Locate every Plasmodium vivax-infected red blood cell.
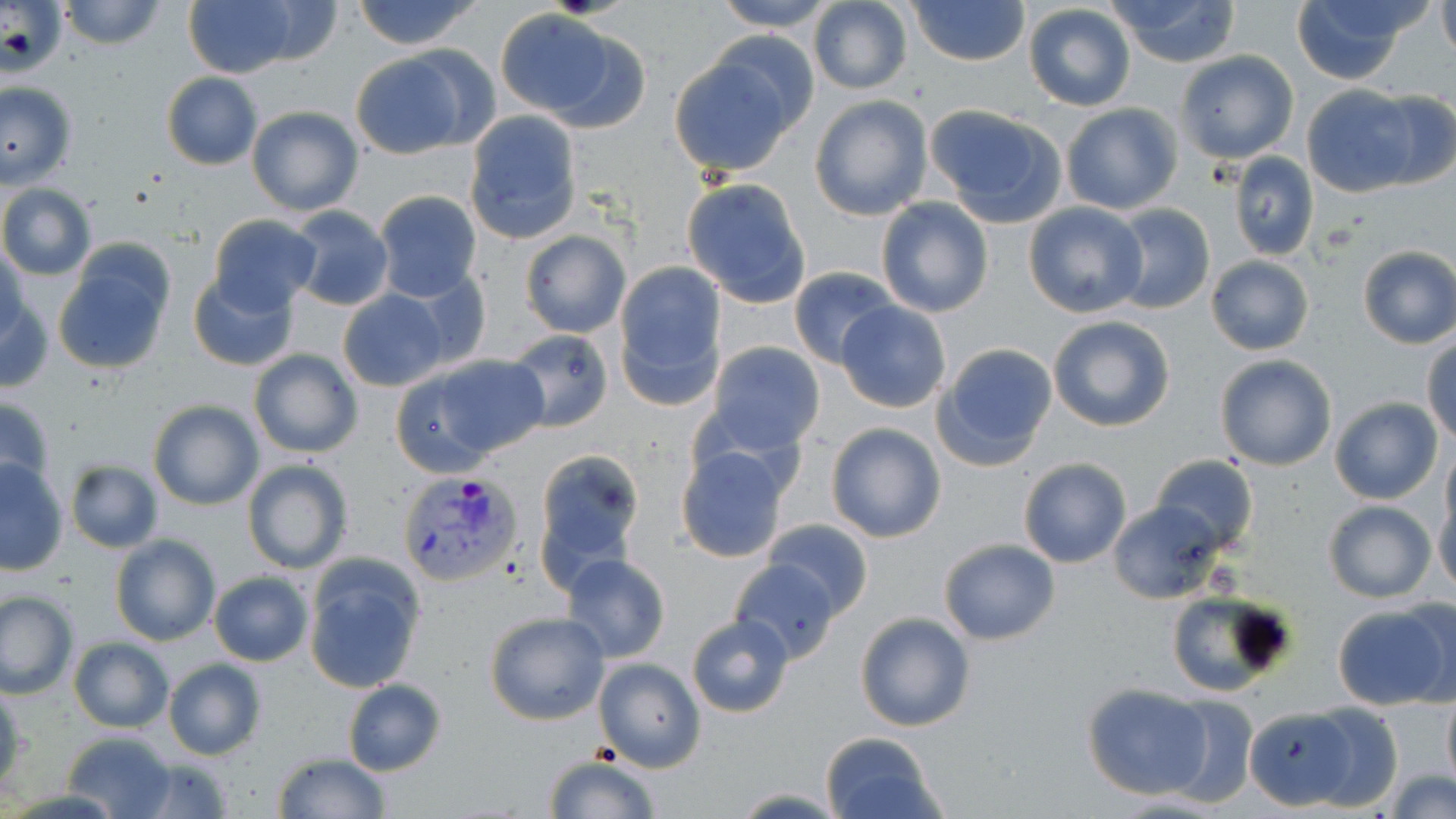
Approximate bounding boxes as named x1/y1/x2/y2 corners in pixels.
Plasmodium vivax-infected red blood cells: (x1=398, y1=471, x2=525, y2=588).

slide_level_diagnosis: Plasmodium vivax
field_of_view: single
uninfected_red_blood_cell_locations: 'approximate bounding boxes as named x1/y1/x2/y2 corners in pixels: (x1=58, y1=0, x2=166, y2=49), (x1=351, y1=0, x2=484, y2=51), (x1=710, y1=0, x2=840, y2=32), (x1=909, y1=0, x2=1029, y2=67), (x1=1108, y1=0, x2=1242, y2=68), (x1=1290, y1=0, x2=1420, y2=85), (x1=806, y1=1, x2=913, y2=93), (x1=1436, y1=1, x2=1456, y2=62), (x1=184, y1=2, x2=298, y2=78), (x1=1023, y1=4, x2=1137, y2=112), (x1=494, y1=13, x2=646, y2=131), (x1=668, y1=49, x2=800, y2=177), (x1=349, y1=50, x2=478, y2=159), (x1=1173, y1=51, x2=1299, y2=165), (x1=161, y1=73, x2=264, y2=170), (x1=0, y1=82, x2=77, y2=188), (x1=1300, y1=85, x2=1424, y2=197), (x1=1361, y1=89, x2=1456, y2=192), (x1=808, y1=95, x2=933, y2=220), (x1=1060, y1=103, x2=1183, y2=215), (x1=925, y1=105, x2=1067, y2=227), (x1=246, y1=106, x2=363, y2=216), (x1=464, y1=111, x2=582, y2=242), (x1=1229, y1=153, x2=1319, y2=261), (x1=682, y1=177, x2=812, y2=308), (x1=1, y1=183, x2=97, y2=280), (x1=373, y1=191, x2=482, y2=301), (x1=875, y1=197, x2=994, y2=317), (x1=1022, y1=201, x2=1149, y2=319), (x1=1106, y1=204, x2=1215, y2=314), (x1=286, y1=206, x2=395, y2=311), (x1=208, y1=215, x2=323, y2=315), (x1=518, y1=231, x2=630, y2=339), (x1=1, y1=246, x2=31, y2=339), (x1=1356, y1=246, x2=1456, y2=349), (x1=52, y1=250, x2=174, y2=374), (x1=1205, y1=255, x2=1314, y2=355), (x1=613, y1=262, x2=726, y2=409), (x1=789, y1=267, x2=902, y2=370), (x1=188, y1=270, x2=299, y2=371), (x1=392, y1=271, x2=492, y2=373), (x1=337, y1=288, x2=450, y2=392), (x1=1, y1=289, x2=52, y2=393), (x1=836, y1=301, x2=951, y2=413), (x1=1047, y1=315, x2=1177, y2=432), (x1=503, y1=328, x2=614, y2=432), (x1=1423, y1=334, x2=1456, y2=445), (x1=708, y1=342, x2=826, y2=454), (x1=932, y1=343, x2=1058, y2=469), (x1=248, y1=349, x2=362, y2=459), (x1=429, y1=354, x2=551, y2=460), (x1=1214, y1=355, x2=1338, y2=471), (x1=388, y1=365, x2=505, y2=478), (x1=0, y1=396, x2=56, y2=498), (x1=1330, y1=398, x2=1443, y2=505), (x1=147, y1=399, x2=263, y2=511), (x1=825, y1=422, x2=946, y2=543), (x1=1442, y1=444, x2=1456, y2=539), (x1=675, y1=446, x2=791, y2=563), (x1=533, y1=450, x2=646, y2=580), (x1=1151, y1=454, x2=1258, y2=554), (x1=1017, y1=458, x2=1132, y2=568), (x1=0, y1=460, x2=69, y2=573), (x1=242, y1=460, x2=354, y2=575), (x1=65, y1=461, x2=163, y2=552), (x1=1433, y1=493, x2=1456, y2=600), (x1=1106, y1=499, x2=1225, y2=605), (x1=1322, y1=499, x2=1437, y2=603), (x1=764, y1=518, x2=873, y2=617), (x1=109, y1=534, x2=220, y2=646), (x1=939, y1=537, x2=1060, y2=645), (x1=300, y1=554, x2=429, y2=693), (x1=561, y1=554, x2=671, y2=663), (x1=730, y1=558, x2=839, y2=663), (x1=208, y1=572, x2=314, y2=667), (x1=1165, y1=589, x2=1293, y2=695), (x1=1, y1=591, x2=78, y2=698), (x1=1395, y1=596, x2=1456, y2=705), (x1=1332, y1=604, x2=1453, y2=711), (x1=484, y1=610, x2=610, y2=725), (x1=855, y1=612, x2=976, y2=732), (x1=686, y1=613, x2=795, y2=717), (x1=69, y1=638, x2=174, y2=731), (x1=592, y1=657, x2=705, y2=772), (x1=162, y1=660, x2=267, y2=761), (x1=343, y1=679, x2=446, y2=776), (x1=1082, y1=682, x2=1215, y2=799), (x1=0, y1=688, x2=27, y2=799), (x1=1441, y1=689, x2=1456, y2=792), (x1=1157, y1=693, x2=1259, y2=808), (x1=1301, y1=705, x2=1405, y2=811), (x1=1245, y1=707, x2=1359, y2=810), (x1=60, y1=732, x2=179, y2=819), (x1=820, y1=732, x2=945, y2=819), (x1=273, y1=753, x2=391, y2=818), (x1=542, y1=754, x2=661, y2=819), (x1=129, y1=756, x2=234, y2=818), (x1=1384, y1=769, x2=1456, y2=819), (x1=726, y1=787, x2=847, y2=818)'
stain: May-Grünwald-Giemsa
preparation: thin blood smear
image_size: 1456×819 pixels
magnification: 1000x
modality: optical microscopy